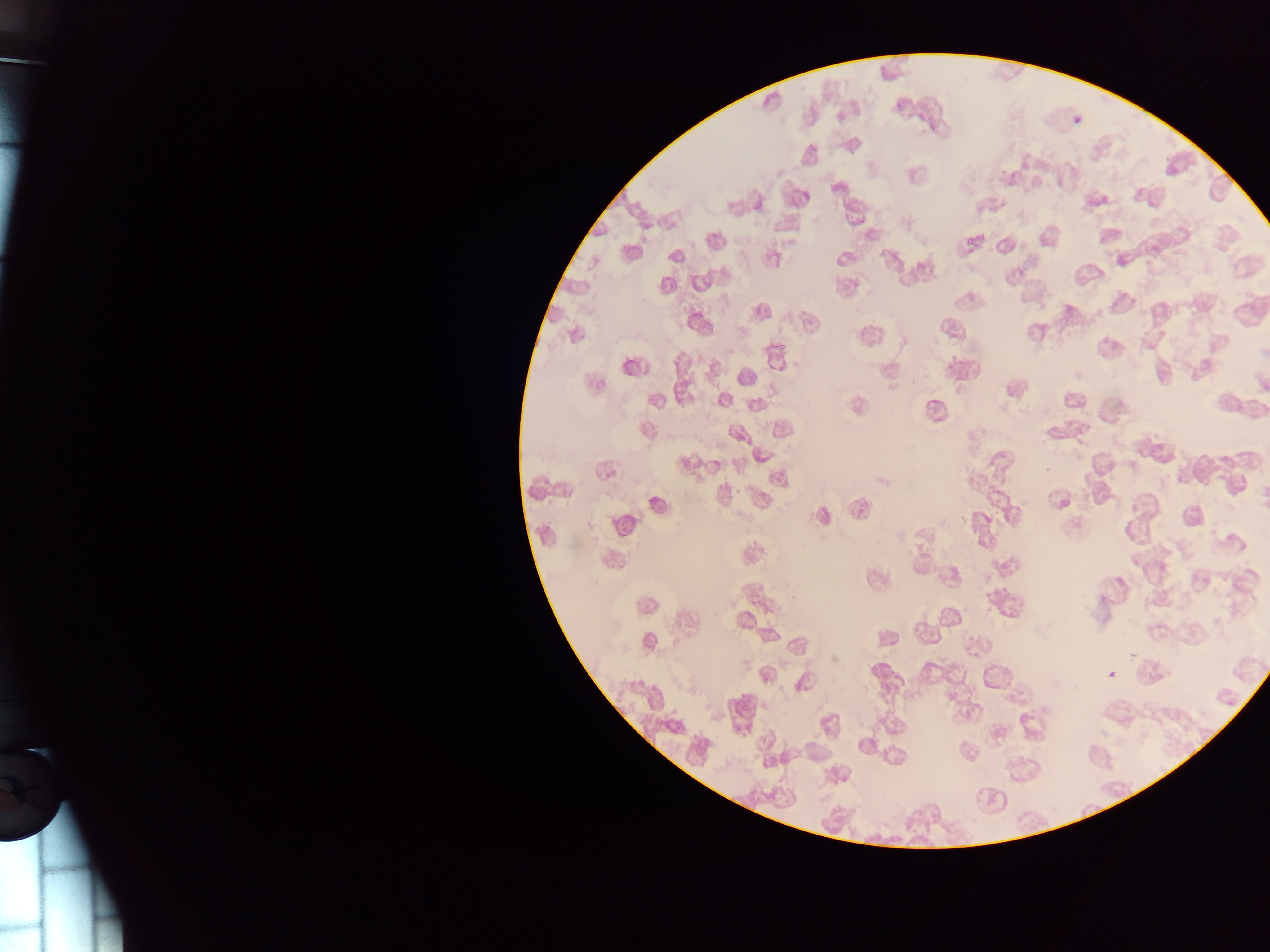
Plasmodium parasite locations = approximate bounding boxes as (left, top, right, bottom) in pixels: (893, 98, 907, 112)
field of view = single
image size = 1270×952 pixels
preparation = thin blood smear
capture = mobile-phone photograph through a microscope
country = Ghana